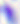

Summary:
  - Modality: photomicrograph
  - Magnification: 400x
  - Identification: Toxoplasma gondii